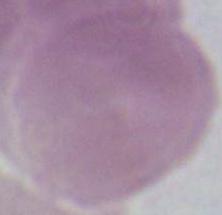

Summary:
  - Modality: micrograph
  - Identification: red blood cell
  - Magnification: 1000x